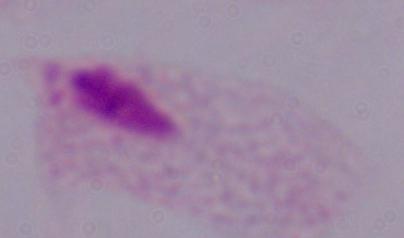

Photomicrograph. A trichomonad is shown. 1000x magnification.